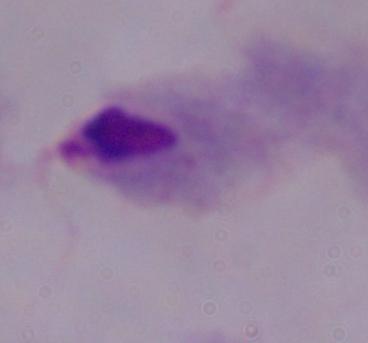

Summary:
  - Modality: micrograph
  - Magnification: 1000x
  - Identification: trichomonad